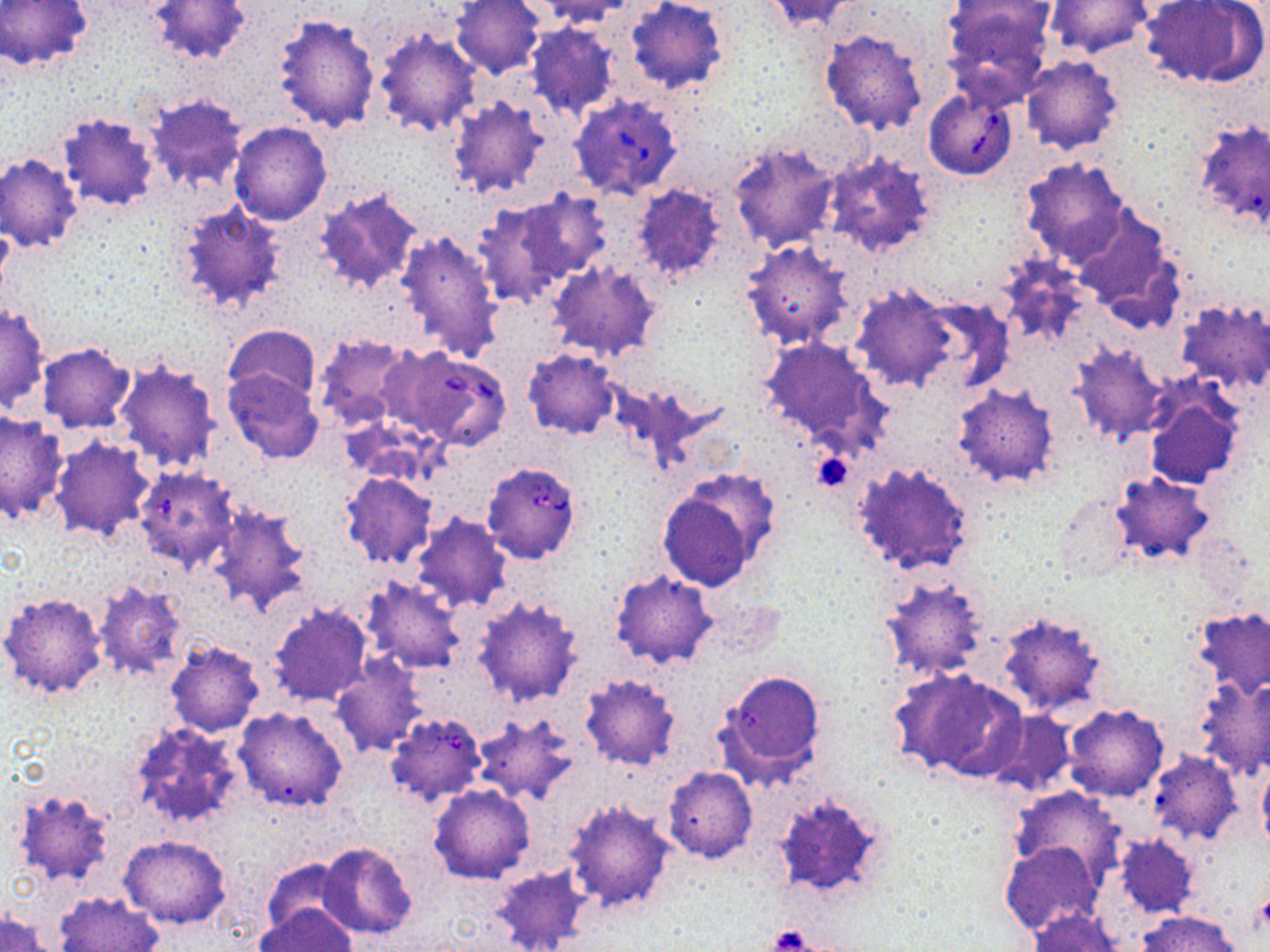

Approximate bounding boxes as named x1/y1/x2/y2 corners in pixels. Uninfected red blood cell locations: (x1=1, y1=0, x2=92, y2=70), (x1=147, y1=0, x2=251, y2=67), (x1=449, y1=0, x2=546, y2=79), (x1=623, y1=0, x2=729, y2=95), (x1=761, y1=0, x2=863, y2=32), (x1=942, y1=0, x2=1056, y2=99), (x1=1137, y1=0, x2=1265, y2=89), (x1=533, y1=1, x2=635, y2=28), (x1=1046, y1=1, x2=1153, y2=59), (x1=272, y1=12, x2=381, y2=134), (x1=526, y1=23, x2=620, y2=122), (x1=372, y1=28, x2=481, y2=138), (x1=818, y1=28, x2=929, y2=135), (x1=1020, y1=55, x2=1124, y2=154), (x1=446, y1=95, x2=552, y2=198), (x1=146, y1=96, x2=248, y2=194), (x1=57, y1=111, x2=160, y2=211), (x1=1191, y1=118, x2=1270, y2=233), (x1=229, y1=120, x2=332, y2=225), (x1=729, y1=142, x2=839, y2=253), (x1=819, y1=149, x2=941, y2=261), (x1=0, y1=152, x2=83, y2=252), (x1=1018, y1=157, x2=1131, y2=268), (x1=628, y1=183, x2=728, y2=288), (x1=313, y1=187, x2=421, y2=294), (x1=511, y1=190, x2=613, y2=284), (x1=474, y1=197, x2=582, y2=307), (x1=172, y1=200, x2=287, y2=314), (x1=1071, y1=207, x2=1185, y2=330), (x1=397, y1=228, x2=504, y2=362), (x1=738, y1=239, x2=856, y2=351), (x1=548, y1=258, x2=663, y2=362), (x1=847, y1=284, x2=960, y2=393), (x1=902, y1=292, x2=1011, y2=395), (x1=1174, y1=298, x2=1270, y2=395), (x1=1, y1=303, x2=49, y2=411), (x1=222, y1=324, x2=321, y2=408), (x1=312, y1=332, x2=421, y2=431), (x1=756, y1=337, x2=889, y2=452), (x1=37, y1=341, x2=137, y2=434), (x1=1068, y1=343, x2=1168, y2=444), (x1=522, y1=347, x2=619, y2=440), (x1=114, y1=360, x2=223, y2=474), (x1=224, y1=369, x2=324, y2=465), (x1=952, y1=383, x2=1061, y2=488), (x1=1145, y1=389, x2=1244, y2=490), (x1=0, y1=410, x2=68, y2=526), (x1=49, y1=436, x2=156, y2=539), (x1=848, y1=461, x2=972, y2=573), (x1=137, y1=464, x2=237, y2=572), (x1=1108, y1=471, x2=1217, y2=566), (x1=339, y1=472, x2=437, y2=568), (x1=656, y1=473, x2=776, y2=592), (x1=1052, y1=493, x2=1130, y2=585), (x1=207, y1=503, x2=314, y2=616), (x1=410, y1=515, x2=511, y2=612), (x1=609, y1=571, x2=718, y2=670), (x1=877, y1=572, x2=992, y2=682), (x1=361, y1=577, x2=467, y2=674), (x1=93, y1=581, x2=187, y2=682), (x1=1, y1=590, x2=108, y2=699), (x1=472, y1=595, x2=584, y2=707), (x1=266, y1=601, x2=374, y2=706), (x1=1189, y1=603, x2=1270, y2=701), (x1=993, y1=609, x2=1113, y2=718), (x1=165, y1=640, x2=264, y2=737), (x1=329, y1=655, x2=427, y2=756), (x1=713, y1=666, x2=829, y2=787), (x1=890, y1=666, x2=1027, y2=782), (x1=579, y1=672, x2=681, y2=772), (x1=1192, y1=676, x2=1270, y2=780), (x1=1063, y1=704, x2=1169, y2=804), (x1=234, y1=705, x2=349, y2=812), (x1=983, y1=709, x2=1075, y2=799), (x1=473, y1=713, x2=580, y2=806), (x1=126, y1=720, x2=246, y2=833), (x1=1147, y1=752, x2=1241, y2=845), (x1=1257, y1=759, x2=1270, y2=854), (x1=662, y1=767, x2=757, y2=863), (x1=429, y1=784, x2=535, y2=884), (x1=1008, y1=785, x2=1123, y2=881), (x1=10, y1=786, x2=119, y2=889), (x1=764, y1=790, x2=891, y2=905), (x1=562, y1=798, x2=676, y2=916), (x1=1113, y1=832, x2=1200, y2=919), (x1=119, y1=835, x2=232, y2=928), (x1=316, y1=840, x2=418, y2=939), (x1=1000, y1=841, x2=1102, y2=936), (x1=261, y1=858, x2=351, y2=941), (x1=490, y1=861, x2=594, y2=952), (x1=55, y1=891, x2=165, y2=952), (x1=257, y1=902, x2=357, y2=950), (x1=1027, y1=907, x2=1124, y2=952), (x1=1136, y1=909, x2=1244, y2=952), (x1=1, y1=911, x2=54, y2=952). Babesia divergens-infected red blood cell locations: (x1=923, y1=86, x2=1020, y2=181), (x1=571, y1=94, x2=683, y2=199), (x1=391, y1=348, x2=512, y2=451), (x1=481, y1=461, x2=583, y2=565), (x1=384, y1=711, x2=488, y2=806). Platelet locations: (x1=812, y1=450, x2=853, y2=492), (x1=768, y1=924, x2=823, y2=950). Slide-level diagnosis: Babesia divergens. Thin blood film. May-Grünwald-Giemsa stain. Image is 1270×952 pixels. 1000x magnification. Optical microscopy. Single field of view.